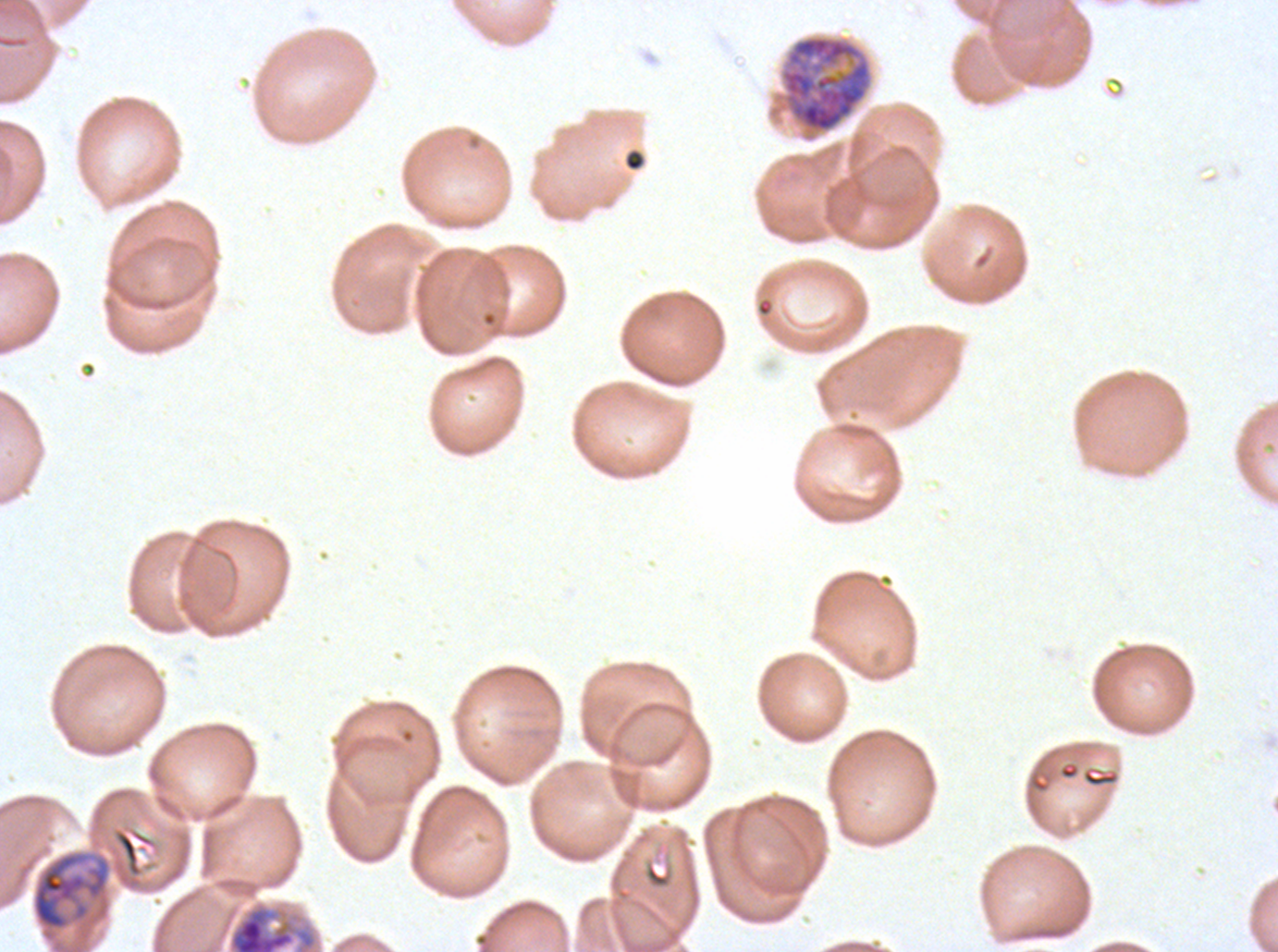

Approximate bounding rectangles given as corner coordinates in pixels from the top-left.
Summary:
  - Late trophozoite locations: (x1=31, y1=849, x2=112, y2=951), (x1=227, y1=899, x2=319, y2=951)
  - Debris locations: (x1=624, y1=150, x2=645, y2=172), (x1=1081, y1=765, x2=1120, y2=788), (x1=644, y1=860, x2=674, y2=889)
  - Early schizont locations: (x1=780, y1=35, x2=872, y2=134)
  - Preparation: thin blood smear
  - Image size: 1278×952 pixels
  - Specimen: Plasmodium falciparum from a patient in The Gambia, cultured ex vivo for 24 to 48 hours
  - Field of view: sub-image separated from a larger composite
  - Life-cycle stages observed: late trophozoite, early schizont
  - Stain: Giemsa